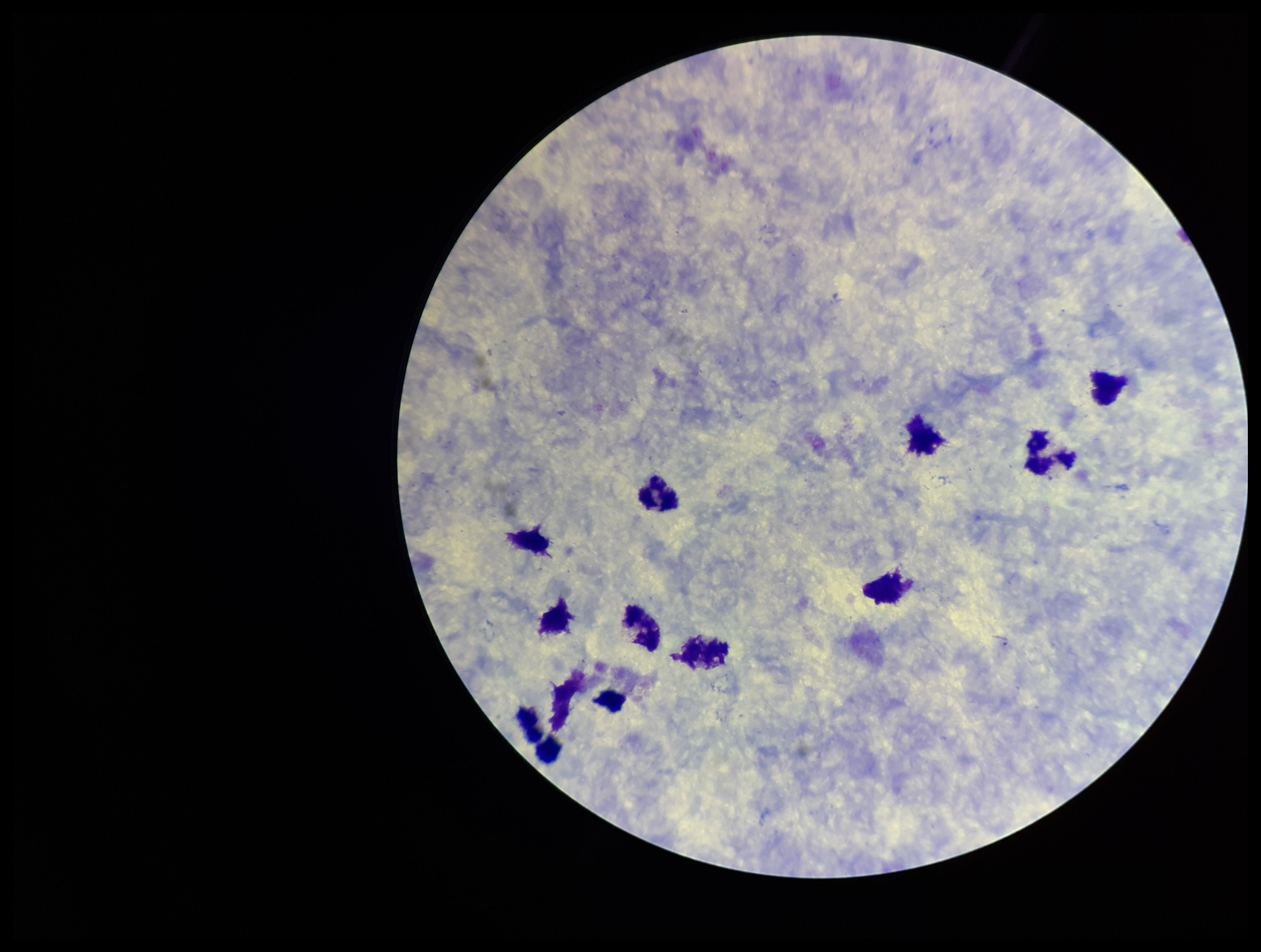
Summary:
  - Patient malaria status: negative
  - Parasite count: 0
  - Plasmodium parasites: none identified
  - Field of view: one from this slide
  - Image size: 1261×952 pixels
  - Stain: Giemsa
  - Capture: smartphone photograph through the microscope eyepiece
  - Leukocyte count: 12
  - Preparation: thick